Identify the parasite.
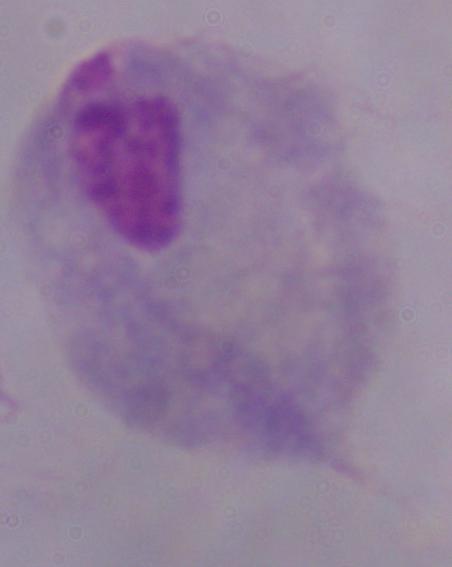

This is a trichomonad.

Summary:
  - Magnification: 1000x
  - Modality: photomicrograph